Classify this cell by malaria status.
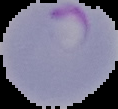

Parasitized.

Summary:
  - Preparation: thin blood film
  - Image type: cell region segmented out of the field of view; surrounding area masked to black
  - Image size: 118×109 pixels